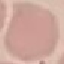

Summary:
  - Malaria status: uninfected
  - Stain: Giemsa
  - Image type: automatically extracted cell patch, resized to 64 × 64 pixels
  - Capture: smartphone camera at the microscope eyepiece
  - Preparation: thin blood film